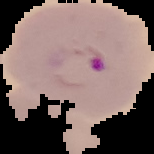
image type = cell region segmented out of the field of view; surrounding area masked to black
preparation = thin blood film
malaria status = parasitized
image size = 154×154 pixels